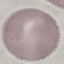
{
  "result": "negative for malaria parasites",
  "image_type": "automatically extracted cell patch, resized to 64 × 64 pixels",
  "capture": "smartphone through the microscope eyepiece",
  "preparation": "thin smear",
  "stain": "Giemsa"
}